Name the cell type shown.
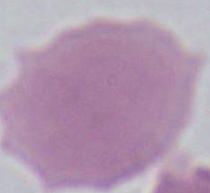
An erythrocyte.

modality = photomicrograph
magnification = 1000x